Locate and identify every blood parasite.
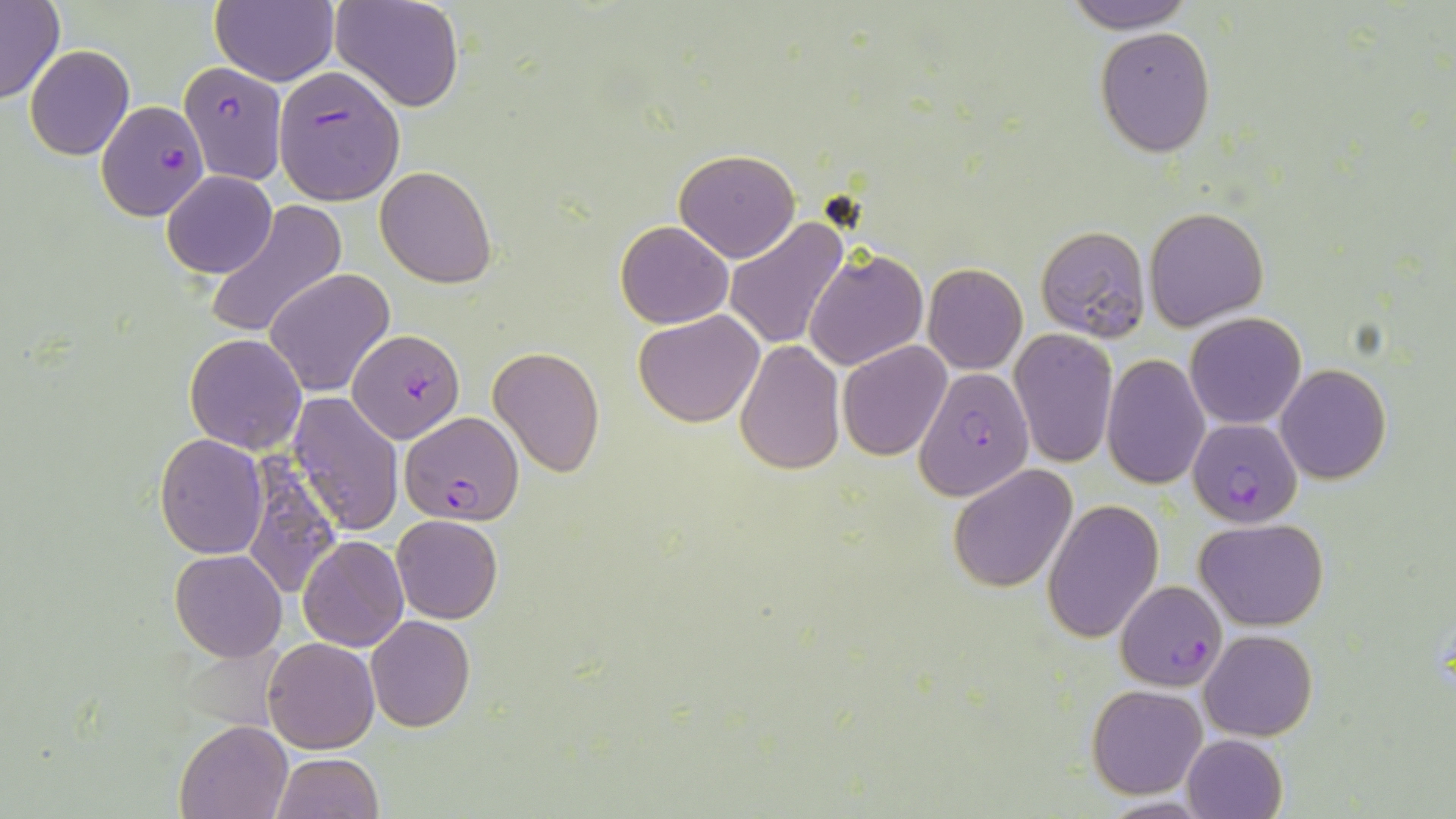
Approximate bounding boxes as (x1,y1)-(x2,y2) corner pairs in pixels.
Plasmodium falciparum-infected red blood cells: (179,62)-(286,185), (273,65)-(405,204), (97,100)-(206,221), (347,329)-(467,444), (914,366)-(1034,499), (401,413)-(525,525), (1188,418)-(1302,526), (1116,579)-(1225,692).
No Plasmodium ovale, Plasmodium malariae, Plasmodium vivax, Babesia divergens, or Trypanosoma brucei observed.

Summary:
  - Uninfected red blood cell locations: (329,0)-(465,112), (1061,0)-(1197,33), (0,2)-(63,104), (210,2)-(338,87), (1095,27)-(1215,157), (25,45)-(134,159), (674,148)-(800,262), (375,166)-(498,287), (163,171)-(277,279), (203,200)-(346,338), (1145,206)-(1270,331), (723,219)-(850,350), (615,221)-(734,329), (1036,225)-(1151,343), (805,250)-(929,371), (922,263)-(1028,375), (265,267)-(395,397), (633,310)-(766,427), (1186,312)-(1307,429), (1009,328)-(1117,468), (185,333)-(308,454), (735,339)-(845,473), (838,341)-(951,460), (490,347)-(605,476), (1101,356)-(1211,489), (1276,365)-(1391,483), (287,392)-(405,537), (154,434)-(268,557), (237,454)-(344,600), (948,465)-(1077,592), (1041,499)-(1163,642), (392,515)-(503,623), (1194,517)-(1330,631), (298,536)-(408,653), (169,549)-(287,661), (365,615)-(477,731), (1200,629)-(1317,741), (263,636)-(380,754), (1087,683)-(1208,799), (174,719)-(291,819), (1182,734)-(1287,819), (271,753)-(384,818), (1100,798)-(1214,818)
  - Slide-level diagnosis: Plasmodium falciparum
  - Field of view: single
  - Image size: 1456×819 pixels
  - Magnification: 1000x
  - Modality: optical microscopy
  - Stain: May-Grünwald-Giemsa
  - Preparation: thin blood film